Point out each Plasmodium parasite.
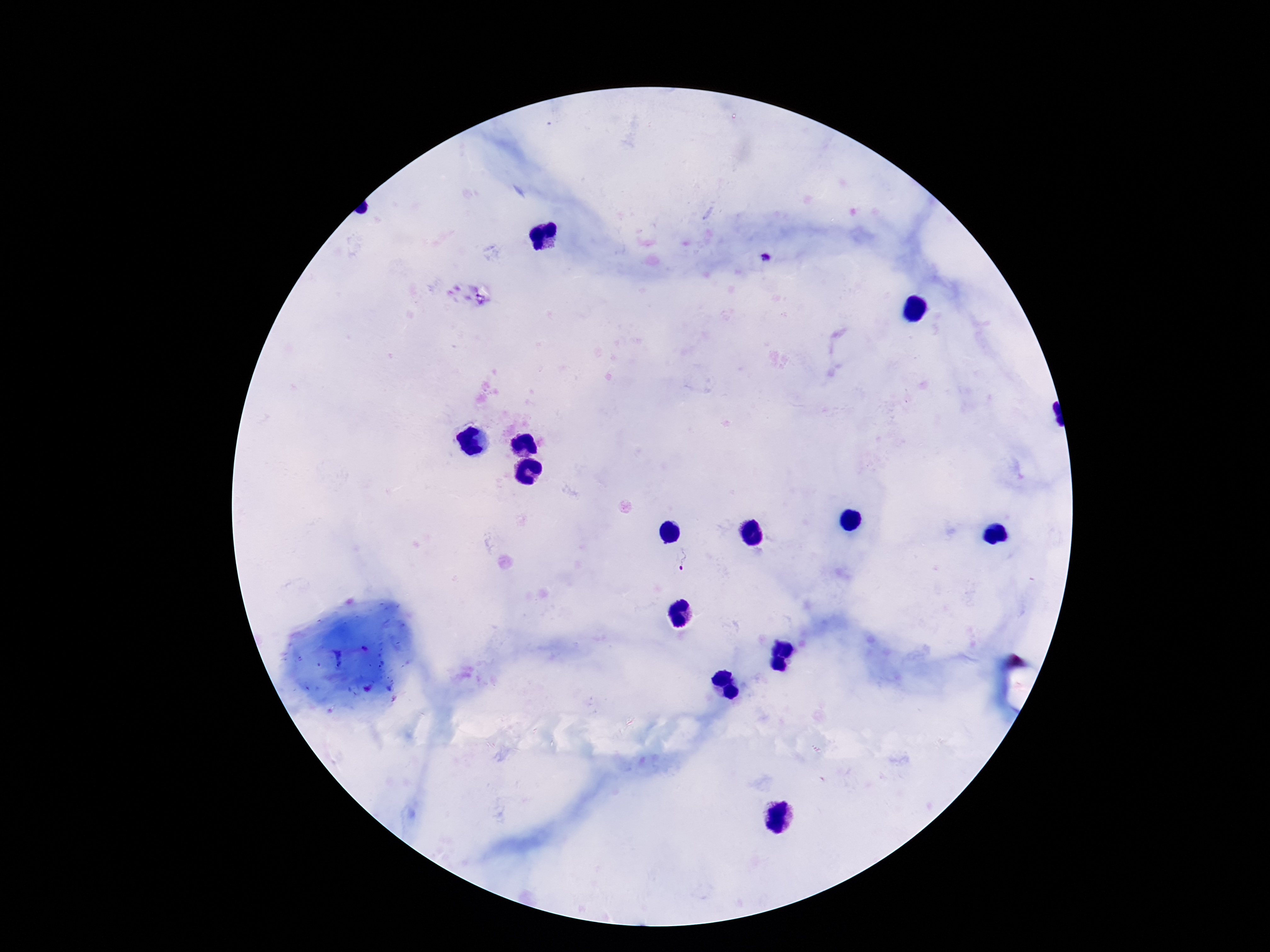

Approximate object centers, in pixels from the top-left corner.
Plasmodium parasites: (x=767, y=258), (x=684, y=563).

Giemsa-stained preparation. One field from this slide. Photographed through the microscope eyepiece with a smartphone camera. Thick peripheral-blood smear. Patient malaria status: infected. Image is 1270×952 pixels. 100x magnification.